Report the malaria status of this cell.
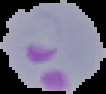

It is parasitized.

From a thin blood film. Image is 106×94 pixels. The area outside the segmented cell region is set to black.